Assess this cell for malaria.
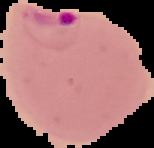
It is parasitized.

Image is 154×148 pixels. Segmented cell region on a black background. From a thin blood film.